Assess this cell for malaria.
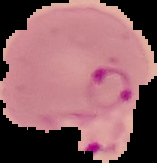

Parasitized.

Image is 157×163 pixels. From a thin blood smear. Cell region segmented out of the field of view; the surrounding area is masked to black.